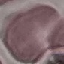
Result: no malaria parasites seen. Giemsa-stained preparation. Thin blood film. Cell patch, automatically extracted from a larger field of view and resized to 64 × 64 pixels. Acquired by smartphone through the microscope eyepiece.